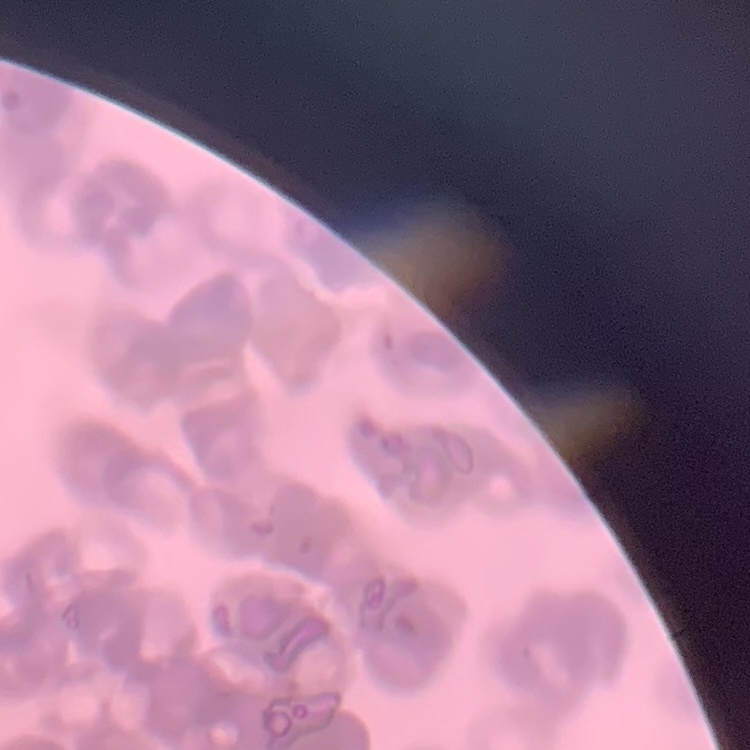

Summary:
  - Red blood cell morphology: rouleaux formation
  - Image type: square crop of a larger photomicrograph
  - Stain: Field's or Giemsa
  - Preparation: thin peripheral smear